Locate every blood parasite and identify its species.
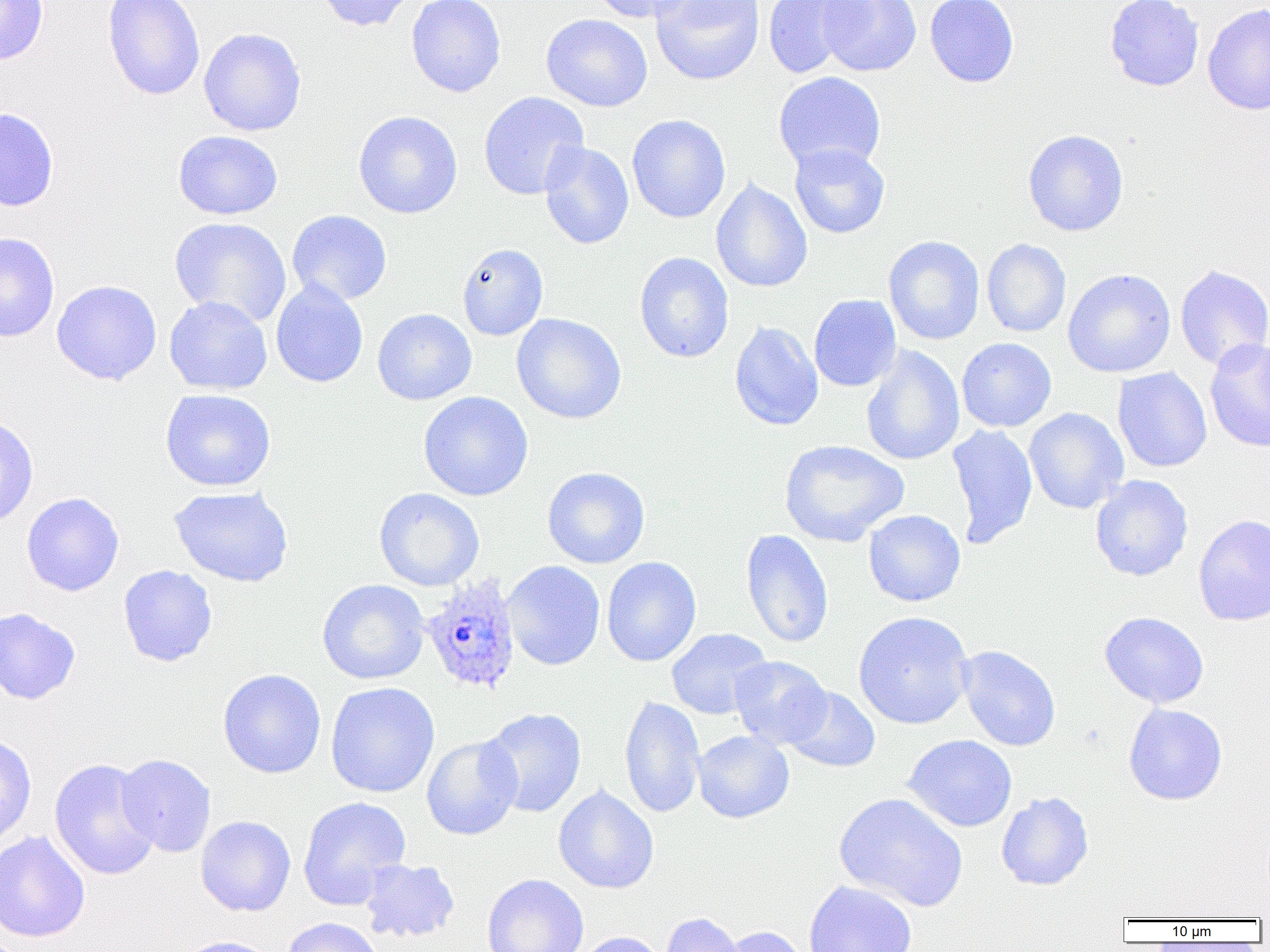

Approximate bounding boxes as (x1,y1)-(x2,y2) corner pairs in pixels.
Plasmodium ovale-infected red blood cells: (420,574)-(522,695).
No Plasmodium falciparum, Plasmodium malariae, Plasmodium vivax, Babesia divergens, or Trypanosoma brucei observed.

slide-level diagnosis = Plasmodium ovale
magnification = 1000x
uninfected red blood cell locations = approximate bounding boxes as (x1,y1)-(x2,y2) corner pairs in pixels: (0,0)-(49,65), (102,0)-(206,100), (314,0)-(417,31), (406,0)-(506,97), (587,0)-(698,23), (651,0)-(766,86), (762,0)-(865,78), (818,0)-(921,77), (925,0)-(1019,88), (1104,0)-(1204,91), (1202,4)-(1270,115), (541,14)-(652,112), (199,27)-(306,136), (773,71)-(886,173), (478,91)-(589,200), (0,106)-(59,212), (353,111)-(463,219), (627,115)-(730,223), (1023,129)-(1129,237), (173,130)-(283,220), (539,141)-(634,249), (789,142)-(890,239), (710,179)-(813,294), (287,209)-(392,306), (169,217)-(292,326), (0,231)-(60,342), (883,235)-(985,345), (982,239)-(1071,337), (457,243)-(548,340), (634,252)-(734,363), (1174,263)-(1270,371), (1063,268)-(1176,378), (51,280)-(162,385), (271,280)-(368,388), (809,294)-(901,392), (164,296)-(273,395), (372,308)-(477,405), (512,313)-(626,424), (729,321)-(824,431), (956,337)-(1057,432), (1204,338)-(1270,452), (861,344)-(965,466), (1112,367)-(1212,473), (160,389)-(276,492), (418,391)-(533,501), (1024,407)-(1129,514), (0,414)-(39,528), (947,423)-(1038,548), (780,439)-(908,547), (542,467)-(650,568), (1090,474)-(1193,581), (169,486)-(294,588), (374,487)-(485,591), (21,492)-(124,597), (863,509)-(966,607), (1193,514)-(1270,626), (740,529)-(834,649), (601,556)-(701,667), (502,560)-(605,671), (118,565)-(218,667), (317,579)-(429,685), (0,607)-(81,705), (853,611)-(974,730), (1099,612)-(1209,708), (666,628)-(772,720), (956,645)-(1061,752), (729,656)-(832,749), (218,668)-(326,779), (325,682)-(440,798), (782,685)-(880,773), (619,694)-(705,819), (1123,703)-(1227,805), (480,707)-(587,817), (692,730)-(794,823), (0,733)-(36,849), (421,734)-(523,840), (902,734)-(1017,832), (116,754)-(216,857), (49,758)-(161,880), (553,785)-(659,894), (834,792)-(968,912), (996,792)-(1094,891), (298,796)-(411,910), (196,815)-(296,917), (0,830)-(90,943), (358,858)-(460,944), (482,874)-(589,952), (804,880)-(918,952), (660,912)-(745,952), (281,916)-(384,952), (718,926)-(809,952), (574,932)-(666,952), (173,936)-(279,952)
image size = 1270×952 pixels
modality = light microscopy
field of view = one of a larger specimen
preparation = thin blood film